Identify the blood parasite species.
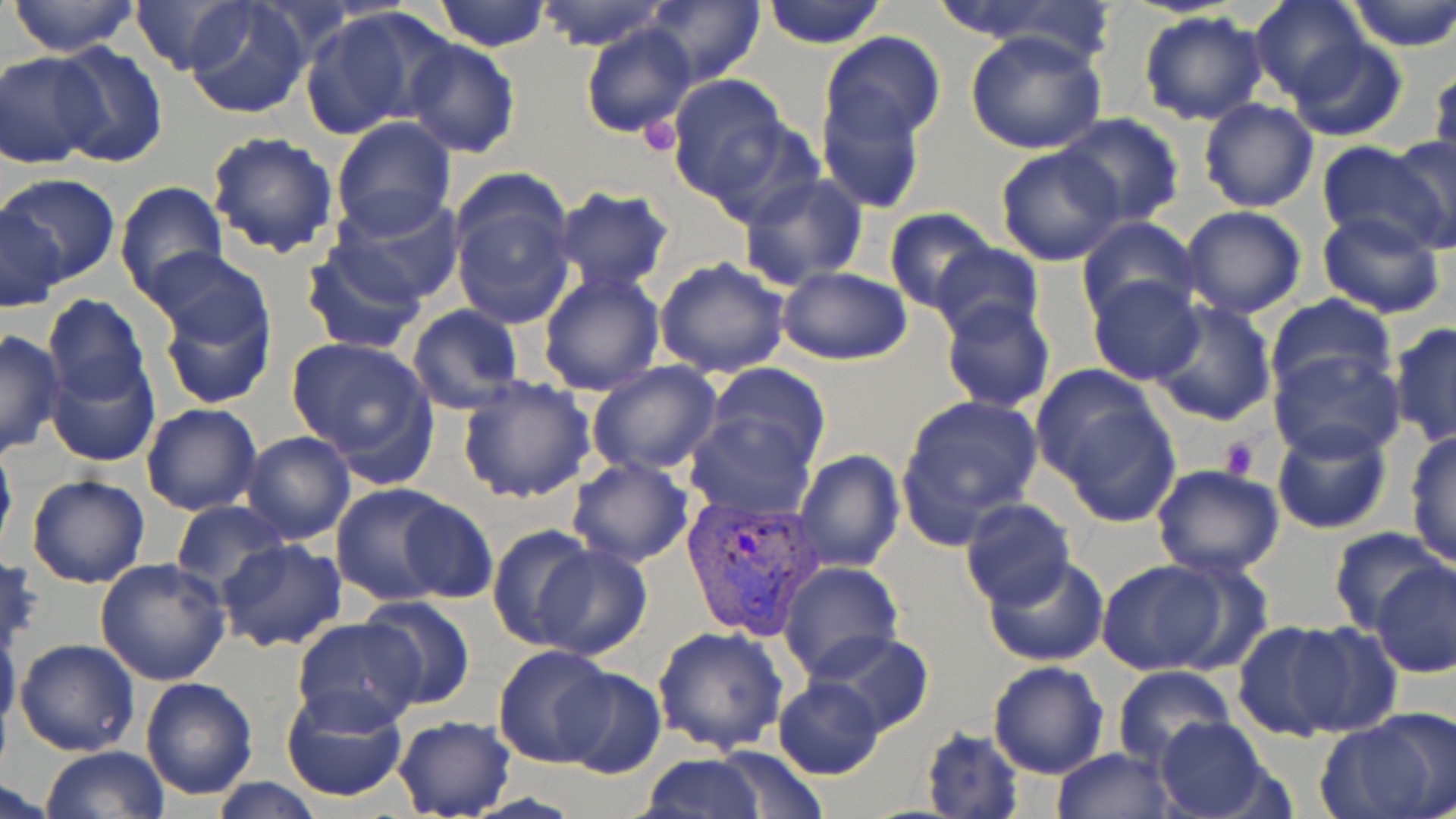

Plasmodium vivax.

modality = optical microscopy
Plasmodium vivax-infected red blood cell locations = approximate bounding boxes as [x1, y1, x2, y2] in pixels: [681, 495, 823, 639]
field of view = single
image size = 1456×819 pixels
stain = May-Grünwald-Giemsa
uninfected red blood cell locations = approximate bounding boxes as [x1, y1, x2, y2] in pixels: [8, 0, 143, 56], [128, 0, 257, 76], [180, 0, 312, 120], [433, 0, 551, 51], [533, 0, 671, 51], [762, 0, 886, 49], [928, 0, 1101, 46], [1343, 0, 1456, 50], [644, 1, 764, 86], [1249, 1, 1370, 104], [300, 8, 440, 140], [1137, 11, 1269, 126], [582, 21, 696, 141], [965, 29, 1108, 155], [820, 31, 947, 148], [402, 36, 520, 157], [1284, 37, 1408, 143], [47, 43, 169, 167], [1, 51, 105, 169], [1430, 61, 1456, 177], [665, 73, 793, 204], [816, 84, 927, 213], [1198, 97, 1319, 213], [1052, 114, 1185, 226], [330, 117, 458, 237], [206, 130, 340, 258], [1386, 131, 1456, 252], [1316, 142, 1447, 252], [995, 145, 1127, 266], [449, 169, 578, 328], [738, 173, 869, 291], [4, 174, 118, 289], [113, 181, 227, 302], [553, 186, 676, 294], [329, 193, 465, 307], [0, 204, 68, 313], [1180, 204, 1308, 319], [884, 209, 997, 314], [1316, 210, 1448, 320], [1076, 216, 1199, 324], [929, 241, 1043, 343], [300, 242, 428, 353], [654, 254, 791, 378], [153, 263, 281, 410], [777, 266, 914, 363], [537, 272, 665, 397], [1087, 275, 1205, 385], [1264, 293, 1396, 401], [40, 294, 153, 411], [938, 298, 1056, 414], [1147, 300, 1277, 427], [407, 305, 524, 414], [1388, 321, 1456, 446], [0, 329, 65, 458], [284, 335, 439, 478], [1271, 347, 1405, 462], [46, 354, 159, 466], [587, 361, 724, 475], [703, 364, 833, 474], [1034, 369, 1180, 522], [456, 374, 596, 502], [897, 393, 1043, 537], [141, 403, 265, 515], [685, 409, 814, 519], [1271, 421, 1394, 536], [1404, 429, 1456, 569], [240, 430, 357, 545], [0, 436, 17, 563], [793, 450, 904, 572], [565, 456, 693, 568], [1151, 463, 1285, 581], [26, 474, 150, 589], [329, 482, 473, 607], [393, 495, 497, 603], [957, 498, 1075, 610], [169, 499, 287, 597], [487, 525, 595, 648], [1330, 526, 1451, 637], [217, 539, 348, 653], [527, 543, 653, 660], [1, 553, 41, 657], [983, 555, 1111, 668], [94, 557, 232, 685], [1370, 559, 1455, 677], [1095, 560, 1236, 674], [778, 561, 904, 683], [357, 597, 475, 711], [291, 618, 426, 733], [1231, 618, 1363, 742], [0, 621, 22, 738], [1282, 621, 1404, 739], [651, 626, 789, 756], [805, 630, 937, 739], [14, 637, 141, 756], [492, 644, 621, 767], [987, 661, 1110, 779], [1113, 666, 1235, 772], [551, 667, 664, 780], [141, 675, 258, 800], [772, 677, 887, 781], [281, 685, 411, 802], [1315, 715, 1450, 819], [392, 716, 515, 818], [1152, 717, 1281, 818], [920, 727, 1023, 818], [708, 744, 830, 818], [41, 745, 170, 819], [1051, 747, 1177, 819], [640, 753, 765, 819], [0, 778, 62, 819], [210, 778, 327, 817]
magnification = 1000x
preparation = thin blood smear
platelet locations = approximate bounding boxes as [x1, y1, x2, y2] in pixels: [638, 117, 683, 156], [1219, 435, 1261, 482]